Report the malaria status of this cell.
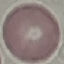

Uninfected.

Summary:
  - Image type: automatically extracted cell patch, resized to 64 × 64 pixels
  - Capture: smartphone camera at the microscope eyepiece
  - Preparation: thin blood film
  - Stain: Giemsa